Assess this cell for malaria.
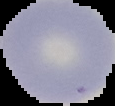

It is uninfected.

image_type: cell region segmented out of the field of view; surrounding area masked to black
preparation: thin blood film
image_size: 115×106 pixels